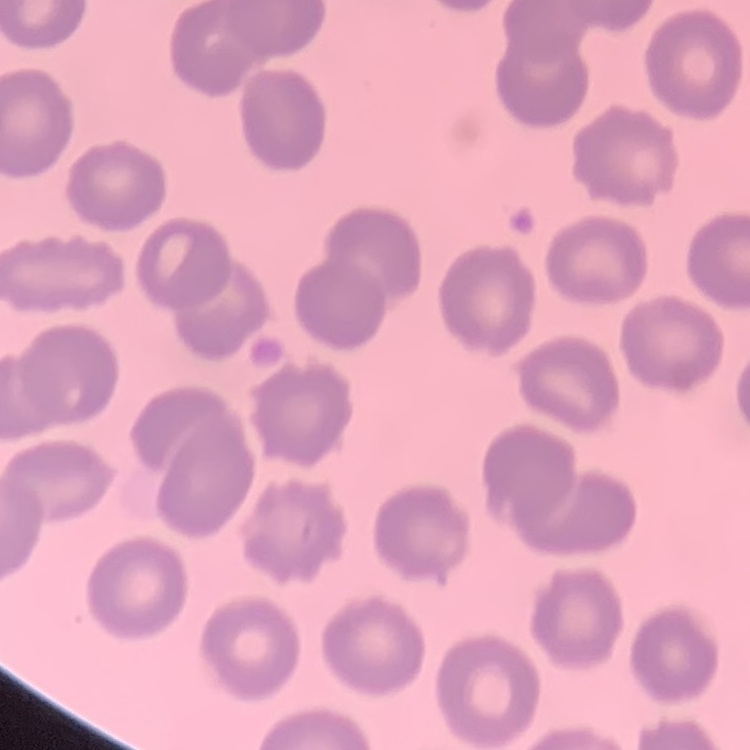

erythrocyte morphology = no rouleaux formation
image type = one tile cut from a larger photomicrograph
stain = Field's or Giemsa
preparation = thin blood smear